Classify this cell by malaria status.
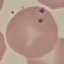
It is parasitized.

capture = smartphone through the microscope eyepiece
image type = automatically extracted cell patch, resized to 64 × 64 pixels
preparation = thin smear
stain = Giemsa